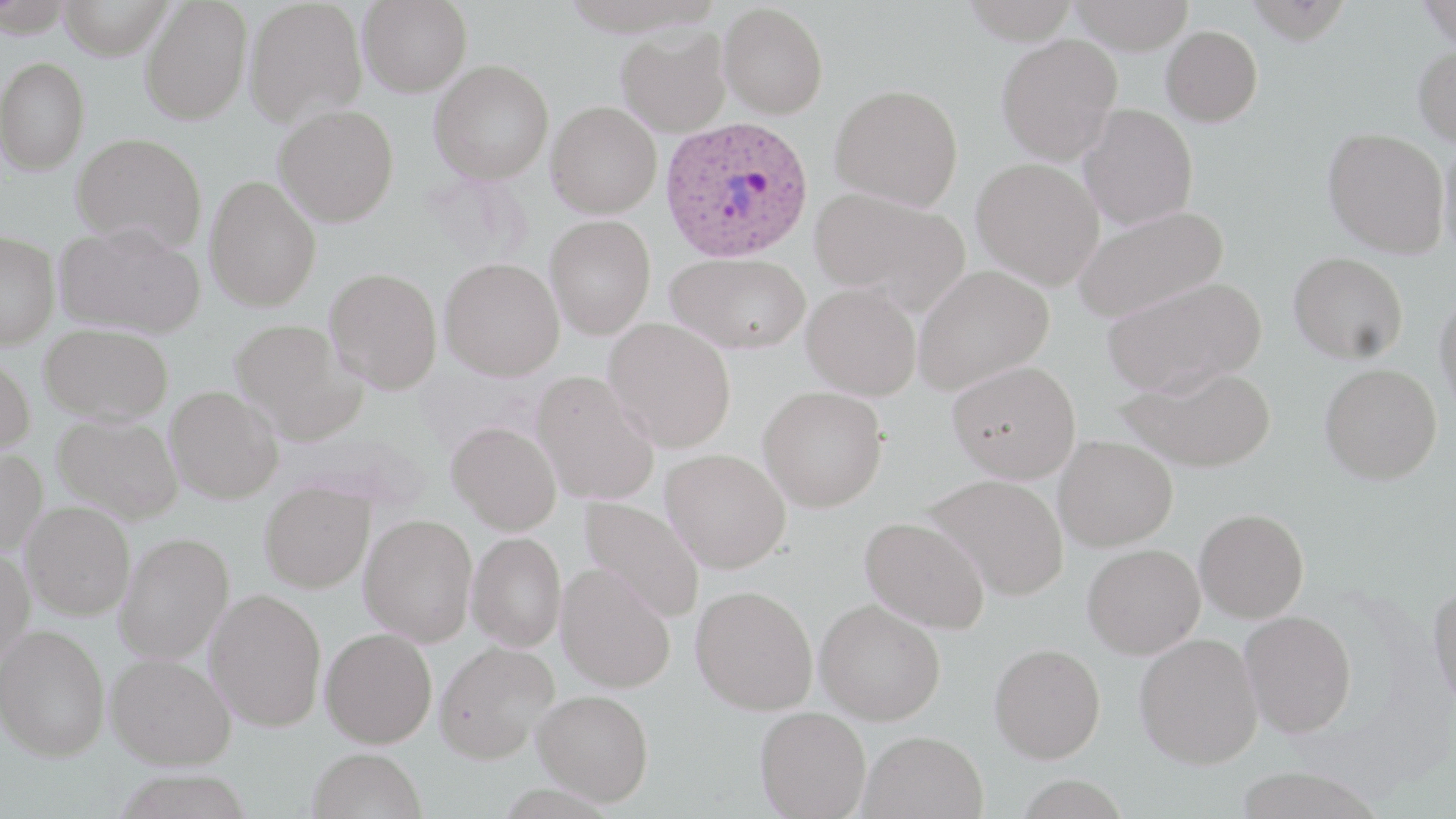

Approximate bounding boxes as (x1,y1)-(x2,y2) corner pairs in pixels. Plasmodium ovale-infected red blood cell locations: (660,115)-(815,262). Uninfected red blood cell locations: (57,0)-(174,59), (140,0)-(252,125), (244,0)-(368,128), (358,0)-(472,98), (961,0)-(1079,44), (1068,0)-(1195,54), (1245,0)-(1351,45), (1416,0)-(1455,49), (719,2)-(829,118), (1161,25)-(1263,126), (616,26)-(732,137), (996,34)-(1122,165), (1413,42)-(1456,147), (0,57)-(90,175), (429,59)-(554,185), (830,83)-(964,210), (547,101)-(661,218), (1078,103)-(1198,230), (273,104)-(399,228), (1322,128)-(1450,257), (72,132)-(208,252), (1438,135)-(1456,263), (971,158)-(1103,290), (204,175)-(321,312), (810,186)-(970,312), (1072,204)-(1228,323), (545,215)-(655,340), (55,220)-(205,338), (0,230)-(59,349), (666,251)-(811,354), (1288,251)-(1408,363), (439,257)-(564,381), (912,264)-(1054,394), (325,268)-(442,394), (1101,275)-(1266,397), (802,282)-(922,400), (1434,291)-(1456,419), (229,318)-(366,444), (604,318)-(736,452), (40,323)-(174,423), (0,357)-(35,458), (948,360)-(1081,483), (1319,362)-(1442,484), (1117,364)-(1276,472), (532,371)-(660,506), (165,386)-(284,504), (758,386)-(888,512), (53,413)-(183,524), (446,421)-(562,535), (1053,435)-(1177,551), (0,446)-(47,556), (660,448)-(791,573), (923,473)-(1069,600), (259,482)-(375,593), (579,497)-(705,621), (21,501)-(134,620), (1194,508)-(1309,622), (359,514)-(477,646), (859,515)-(990,634), (114,532)-(234,665), (467,532)-(566,652), (1082,543)-(1205,659), (0,548)-(34,670), (556,563)-(676,693), (1428,581)-(1456,712), (690,584)-(818,715), (204,588)-(327,732), (815,599)-(945,725), (1239,610)-(1357,737), (0,625)-(109,761), (320,627)-(437,748), (1134,632)-(1263,769), (434,640)-(560,764), (989,643)-(1106,763), (106,653)-(235,770), (532,689)-(654,806), (755,706)-(871,818), (858,730)-(988,819), (308,747)-(427,819), (1233,765)-(1385,818). Slide-level diagnosis: Plasmodium ovale. Captured at 1000x magnification. May-Grünwald-Giemsa-stained preparation. Single field of view. Optical microscopy. Image is 1456×819 pixels. Thin blood film.